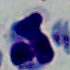

Summary:
  - Modality: micrograph
  - Identification: leukocyte
  - Magnification: 1000x